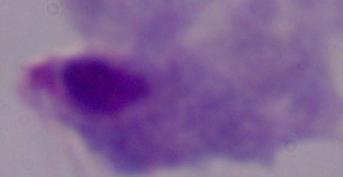 A trichomonad is seen. Micrograph. Captured at 1000x magnification.